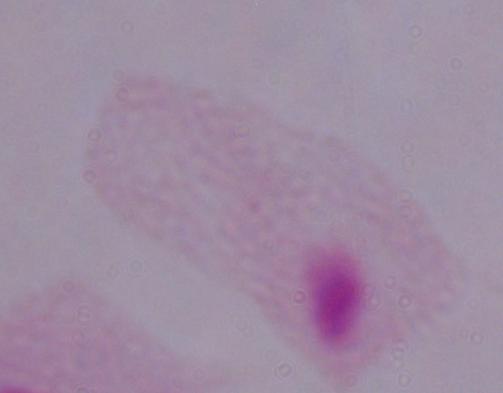
Summary:
  - Modality: micrograph
  - Magnification: 1000x
  - Identification: trichomonad